Classify this cell by malaria status.
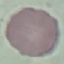
Uninfected.

Summary:
  - Stain: Giemsa
  - Capture: smartphone camera at the microscope eyepiece
  - Image type: cell patch, automatically extracted from a larger field of view and resized to 64 × 64 pixels
  - Preparation: thin blood smear